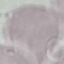 Result: no malaria parasites seen. Giemsa stain. Thin blood smear. Cell patch, automatically extracted from a larger field of view and resized to 64 × 64 pixels. Acquired by smartphone through the microscope eyepiece.